Classify this cell by malaria status.
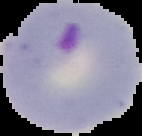
Parasitized.

Summary:
  - Image type: segmented cell region on a black background
  - Image size: 142×136 pixels
  - Preparation: thin blood film